Report the malaria status of this cell.
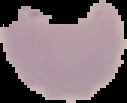

It is uninfected.

From a thin blood smear. The area outside the segmented cell region is set to black. Image is 127×103 pixels.